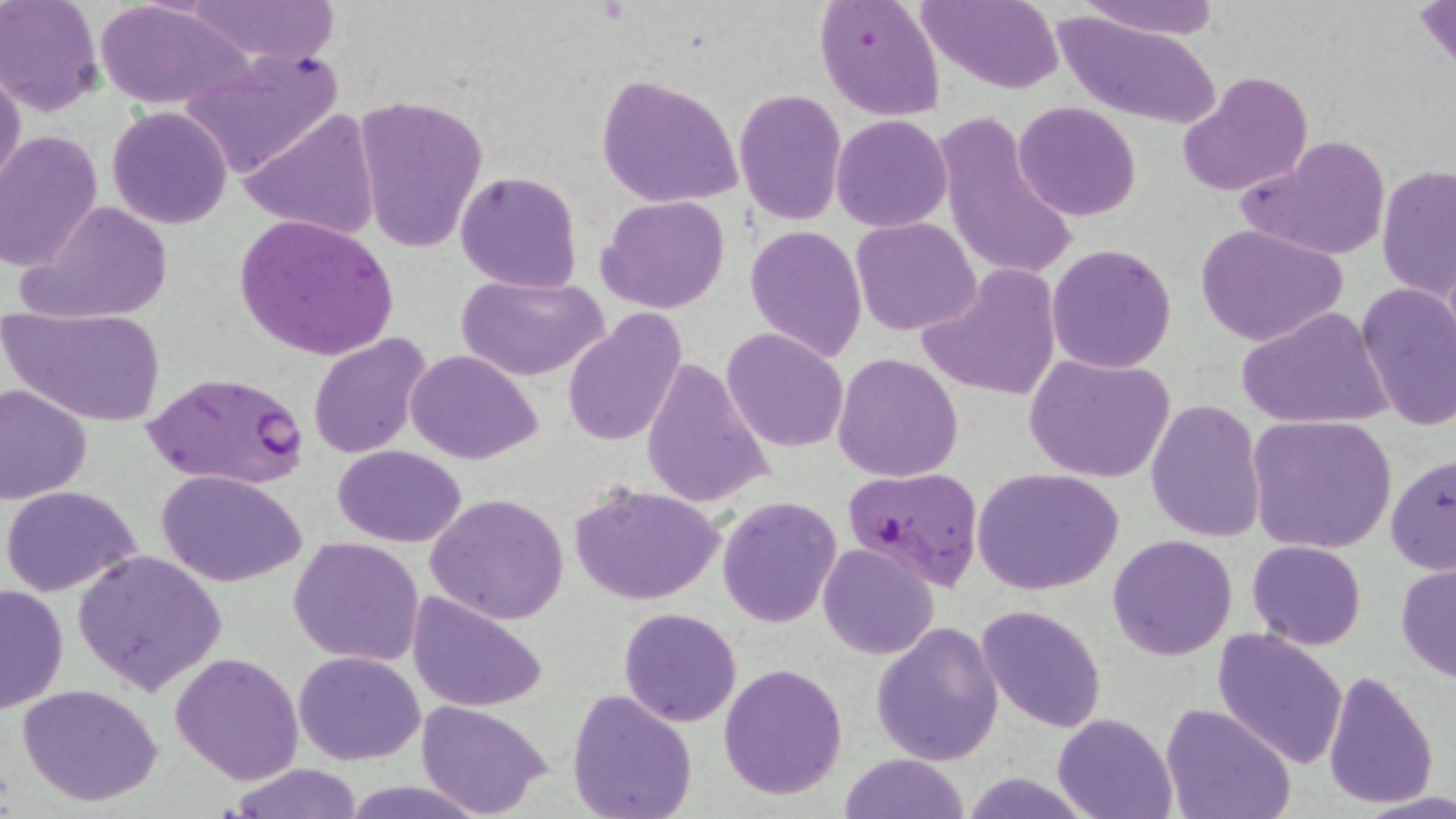
Approximate bounding boxes as named x1/y1/x2/y2 corners in pixels. Uninfected red blood cell locations: (x1=1, y1=0, x2=104, y2=115), (x1=96, y1=0, x2=256, y2=112), (x1=178, y1=0, x2=343, y2=67), (x1=814, y1=0, x2=947, y2=121), (x1=916, y1=0, x2=1064, y2=93), (x1=1076, y1=0, x2=1221, y2=37), (x1=1415, y1=1, x2=1456, y2=79), (x1=1051, y1=10, x2=1220, y2=128), (x1=179, y1=43, x2=346, y2=178), (x1=0, y1=63, x2=25, y2=199), (x1=1177, y1=69, x2=1314, y2=196), (x1=597, y1=73, x2=743, y2=210), (x1=733, y1=88, x2=846, y2=225), (x1=355, y1=92, x2=487, y2=253), (x1=1013, y1=102, x2=1141, y2=221), (x1=107, y1=106, x2=232, y2=229), (x1=239, y1=108, x2=381, y2=243), (x1=831, y1=114, x2=953, y2=233), (x1=937, y1=114, x2=1079, y2=286), (x1=0, y1=129, x2=104, y2=271), (x1=1239, y1=133, x2=1392, y2=262), (x1=1377, y1=164, x2=1455, y2=306), (x1=454, y1=170, x2=584, y2=294), (x1=598, y1=194, x2=731, y2=313), (x1=20, y1=199, x2=176, y2=325), (x1=234, y1=213, x2=402, y2=363), (x1=852, y1=218, x2=982, y2=335), (x1=1194, y1=222, x2=1349, y2=347), (x1=746, y1=224, x2=869, y2=362), (x1=1047, y1=242, x2=1178, y2=373), (x1=918, y1=261, x2=1062, y2=403), (x1=457, y1=274, x2=606, y2=382), (x1=1354, y1=284, x2=1456, y2=433), (x1=1238, y1=305, x2=1393, y2=431), (x1=3, y1=306, x2=164, y2=429), (x1=561, y1=309, x2=688, y2=447), (x1=722, y1=328, x2=849, y2=452), (x1=308, y1=333, x2=434, y2=460), (x1=405, y1=348, x2=543, y2=464), (x1=832, y1=351, x2=963, y2=482), (x1=1023, y1=352, x2=1175, y2=483), (x1=640, y1=356, x2=775, y2=508), (x1=0, y1=382, x2=93, y2=503), (x1=1147, y1=399, x2=1266, y2=544), (x1=1247, y1=415, x2=1397, y2=557), (x1=333, y1=444, x2=468, y2=547), (x1=1384, y1=451, x2=1454, y2=575), (x1=972, y1=467, x2=1124, y2=594), (x1=157, y1=469, x2=305, y2=587), (x1=570, y1=481, x2=724, y2=608), (x1=1, y1=484, x2=144, y2=597), (x1=426, y1=493, x2=570, y2=626), (x1=716, y1=495, x2=841, y2=628), (x1=1106, y1=534, x2=1238, y2=661), (x1=288, y1=536, x2=425, y2=667), (x1=1246, y1=540, x2=1367, y2=649), (x1=817, y1=543, x2=940, y2=660), (x1=73, y1=548, x2=229, y2=695), (x1=1394, y1=562, x2=1455, y2=683), (x1=0, y1=583, x2=69, y2=714), (x1=407, y1=591, x2=549, y2=713), (x1=975, y1=603, x2=1107, y2=732), (x1=618, y1=607, x2=743, y2=728), (x1=870, y1=621, x2=1006, y2=766), (x1=1210, y1=627, x2=1350, y2=769), (x1=294, y1=650, x2=425, y2=765), (x1=170, y1=652, x2=304, y2=784), (x1=719, y1=662, x2=849, y2=799), (x1=1322, y1=670, x2=1440, y2=808), (x1=17, y1=683, x2=162, y2=807), (x1=567, y1=687, x2=698, y2=819), (x1=413, y1=700, x2=554, y2=818), (x1=1159, y1=701, x2=1297, y2=819), (x1=1052, y1=713, x2=1177, y2=819), (x1=836, y1=753, x2=974, y2=818), (x1=225, y1=765, x2=369, y2=819), (x1=961, y1=773, x2=1092, y2=817), (x1=1356, y1=794, x2=1456, y2=819). Plasmodium falciparum-infected red blood cell locations: (x1=140, y1=369, x2=313, y2=489), (x1=840, y1=465, x2=985, y2=591). Slide-level diagnosis: Plasmodium falciparum. Image is 1456×819 pixels. One field of a larger specimen. 1000x magnification. Optical microscopy. Thin blood film. May-Grünwald-Giemsa stain.